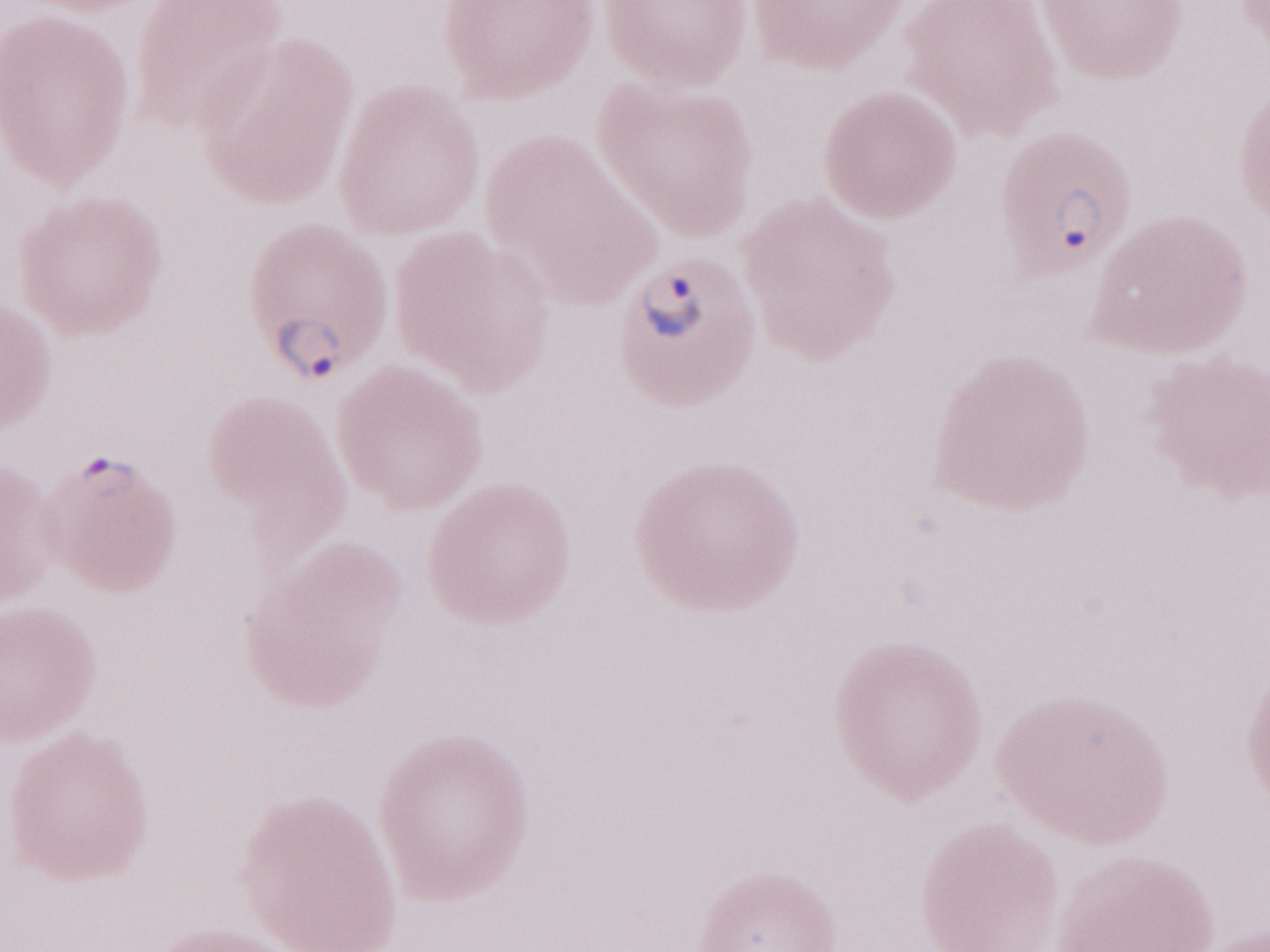 Magnification: 1,000x. Thin blood film. May-Grünwald-Giemsa (MGG) stain. Patient diagnosis: malaria infection. One field of this slide. Olympus BX43 microscope and DP73 digital camera. Image is 1270×952 pixels.